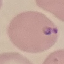 Result: malaria parasites detected. Thin blood smear. Giemsa-stained preparation. Photographed with a smartphone camera at the microscope eyepiece. Automatically extracted cell patch, resized to 64 × 64 pixels.